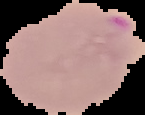 Result: malaria parasites identified. From a thin blood smear. Image is 145×115 pixels. The area outside the segmented cell region is set to black.